Classify this cell by malaria status.
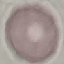

It is uninfected.

Giemsa-stained preparation. Thin smear of blood. Automatically extracted cell patch, resized to 64 × 64 pixels. Photographed with a smartphone camera at the microscope eyepiece.